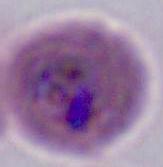
Captured at either 400x or 1000x magnification. A Plasmodium parasite is shown. Micrograph.